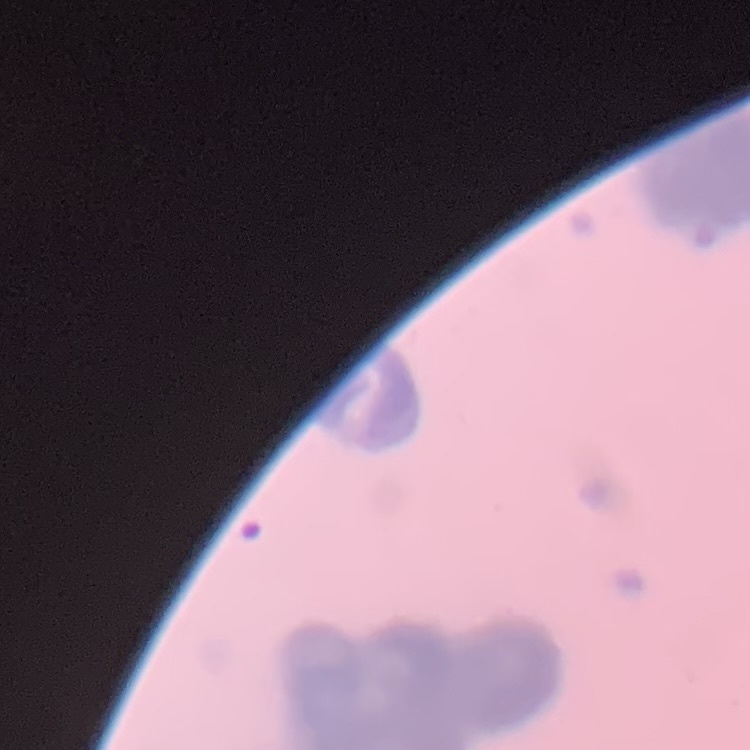

red blood cell morphology = rouleaux formation
stain = Field's or Giemsa
preparation = thin blood smear
image type = one tile cut from a larger photomicrograph